Outline each Plasmodium vivax-infected red blood cell.
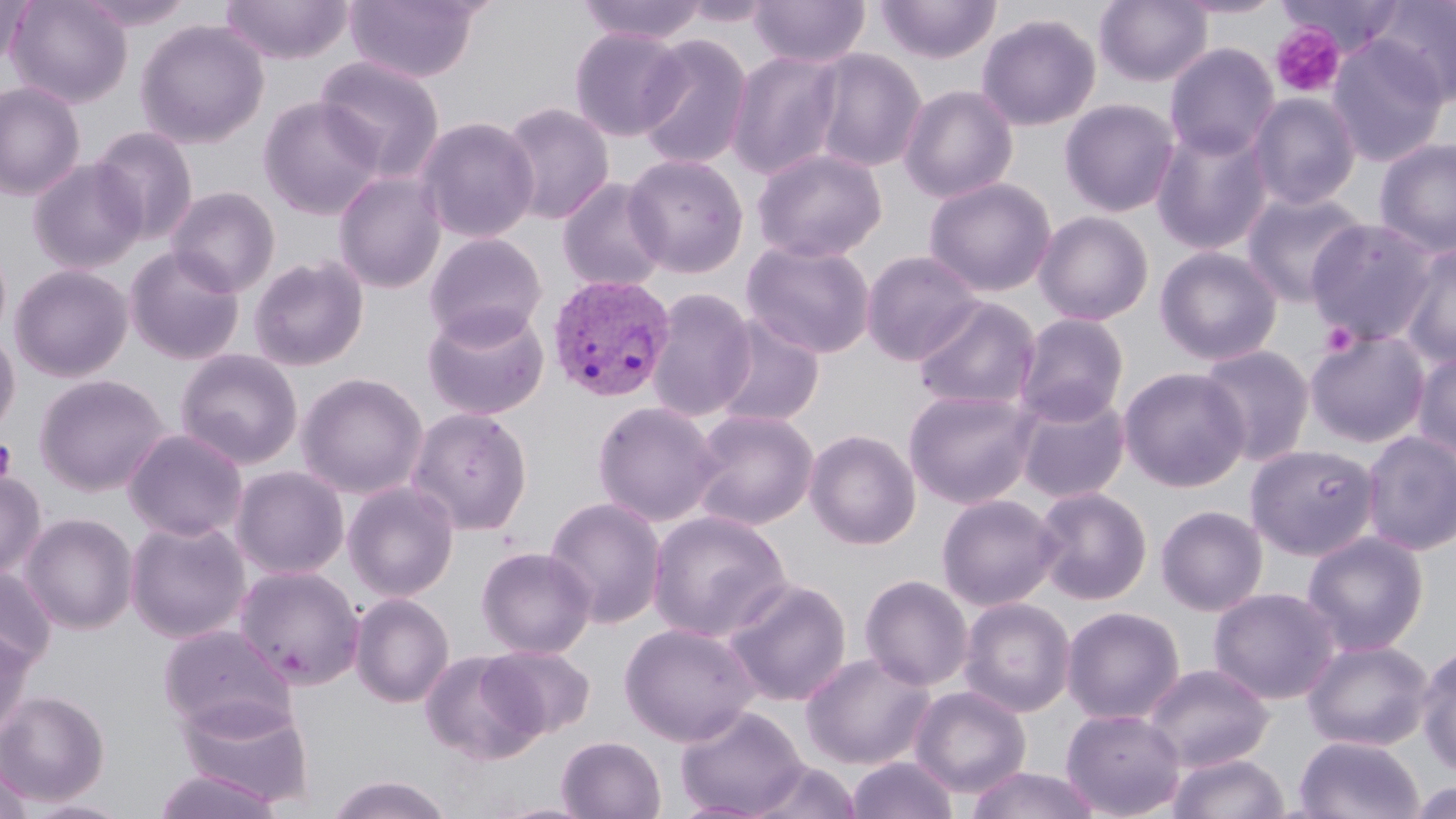
Approximate bounding boxes as (x1,y1)-(x2,y2) corner pairs in pixels.
Plasmodium vivax-infected red blood cells: (547,274)-(675,402).

Uninfected red blood cell locations: (0,0)-(32,70), (6,0)-(133,109), (75,0)-(197,32), (219,0)-(354,64), (345,0)-(483,83), (576,0)-(710,45), (678,0)-(778,28), (749,0)-(871,68), (875,0)-(1001,64), (1094,0)-(1213,87), (1172,0)-(1288,19), (1277,0)-(1406,56), (1369,0)-(1456,106), (976,13)-(1102,131), (135,19)-(270,149), (569,26)-(687,141), (635,33)-(754,170), (1326,35)-(1450,167), (1164,43)-(1280,161), (807,48)-(927,173), (726,50)-(845,179), (314,55)-(446,180), (0,81)-(86,201), (898,84)-(1018,203), (1247,92)-(1362,211), (257,96)-(385,220), (1059,98)-(1180,217), (499,101)-(615,225), (415,116)-(540,244), (1150,124)-(1274,255), (89,126)-(200,244), (1373,137)-(1456,258), (752,147)-(888,263), (623,153)-(749,278), (27,158)-(146,273), (333,170)-(446,293), (923,176)-(1057,297), (556,177)-(670,293), (165,185)-(281,297), (1240,189)-(1370,307), (1033,210)-(1155,326), (1306,220)-(1439,346), (423,233)-(547,345), (741,239)-(877,359), (1398,243)-(1456,369), (1154,245)-(1283,366), (124,246)-(246,365), (861,250)-(983,365), (248,254)-(370,372), (9,263)-(133,382), (647,287)-(758,422), (912,296)-(1042,412), (422,305)-(549,420), (1013,313)-(1130,426), (711,316)-(825,429), (0,328)-(21,438), (1305,329)-(1430,448), (1198,345)-(1316,466), (175,348)-(303,469), (1413,349)-(1456,461), (1119,367)-(1250,492), (296,371)-(429,499), (34,373)-(170,497), (903,388)-(1039,508), (1013,390)-(1131,504), (591,400)-(723,526), (406,407)-(533,534), (688,408)-(819,530), (123,428)-(249,542), (805,428)-(921,549), (1361,430)-(1456,556), (1245,443)-(1380,560), (231,465)-(350,579), (0,470)-(46,582), (342,480)-(460,601), (1032,486)-(1153,605), (936,493)-(1061,611), (544,496)-(667,628), (1155,505)-(1268,616), (647,510)-(792,642), (21,513)-(138,634), (126,517)-(251,643), (1302,531)-(1429,655), (475,545)-(596,658), (233,564)-(365,690), (0,566)-(57,674), (859,574)-(974,691), (721,577)-(853,706), (1208,586)-(1341,704), (350,592)-(455,708), (958,596)-(1076,717), (1061,606)-(1185,725), (619,622)-(759,745), (156,623)-(295,735), (0,628)-(35,740), (1301,638)-(1434,751), (481,645)-(596,739), (1416,646)-(1456,778), (419,649)-(544,765), (799,651)-(935,770), (1142,662)-(1274,772), (909,685)-(1031,798), (0,690)-(110,806), (175,696)-(315,808), (675,705)-(808,817), (1061,708)-(1185,818), (557,735)-(666,819), (1294,735)-(1424,819), (1167,752)-(1289,819), (847,756)-(957,818), (748,759)-(863,819), (0,760)-(36,818), (965,767)-(1103,819), (151,768)-(285,819), (324,775)-(455,818), (1406,783)-(1453,819), (21,798)-(136,819). Platelet locations: (1270,23)-(1346,99), (1320,321)-(1359,357), (0,439)-(17,484). Slide-level diagnosis: Plasmodium vivax. Light microscopy. Image is 1456×819 pixels. Captured at 1000x magnification. May-Grünwald-Giemsa stain. Thin blood film. Single field of view.